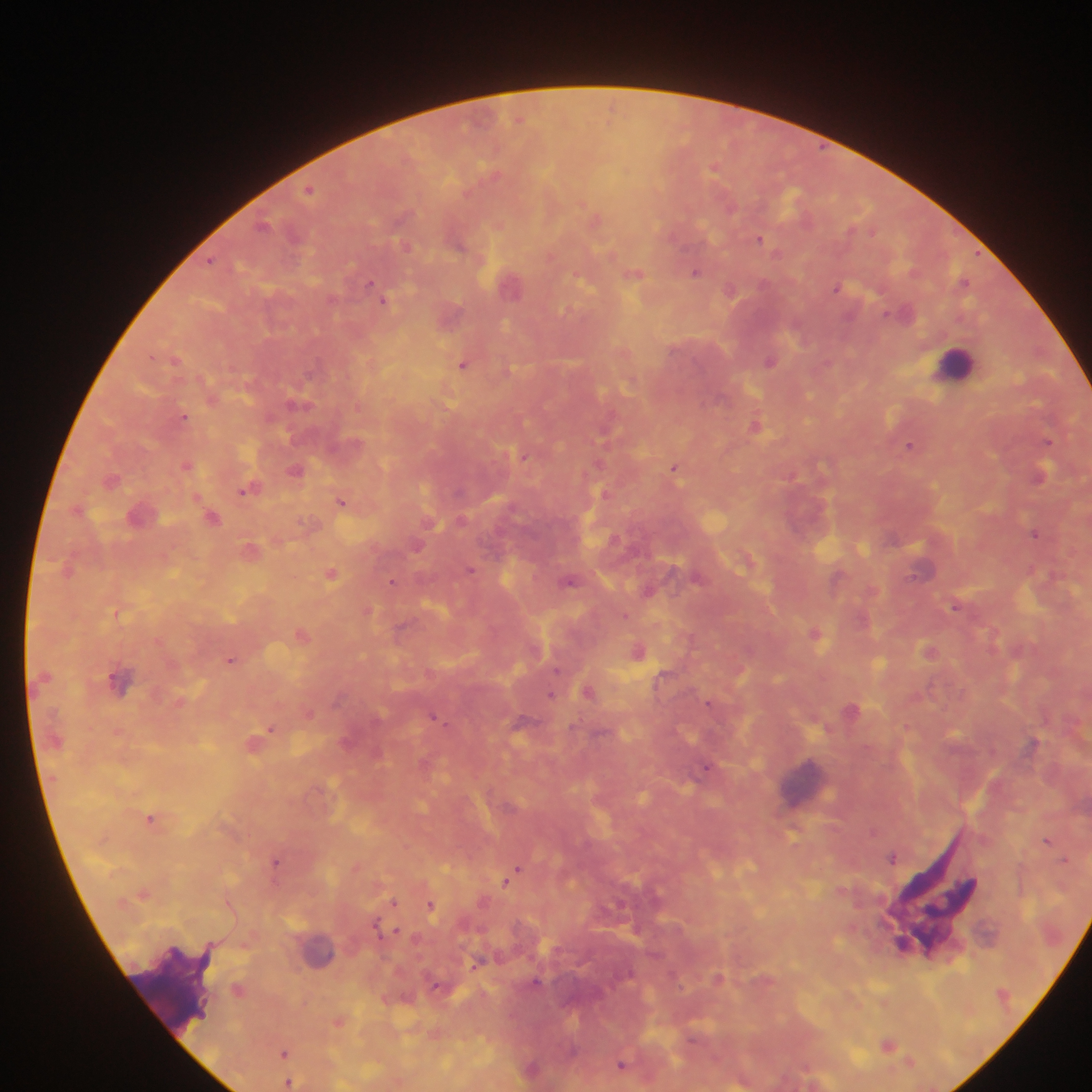

leukocyte locations = approximate centers as [x, y] in pixels: [955, 361], [120, 680], [807, 783], [322, 952], [171, 997]
image size = 1092×1092 pixels
country = Ghana
preparation = thick blood film
Plasmodium parasite locations = approximate centers as [x, y] in pixels: [611, 106], [520, 119], [715, 168], [309, 189], [731, 208], [262, 225], [759, 238], [457, 244], [405, 246], [211, 260], [695, 272], [634, 274], [965, 281], [369, 284], [512, 287], [836, 288], [730, 290], [384, 301], [176, 359], [771, 360], [462, 364], [296, 405], [183, 416], [754, 426], [1047, 441], [909, 446], [524, 456], [187, 465], [674, 467], [295, 470], [1041, 476], [111, 480], [246, 489], [341, 501], [212, 517], [1034, 533], [416, 547], [470, 569], [332, 573], [696, 576], [837, 578], [392, 581], [570, 582], [648, 591], [955, 607], [368, 611], [626, 615], [815, 633], [302, 635], [638, 651], [929, 651], [231, 660], [557, 670], [589, 692], [551, 694], [709, 703], [433, 716], [520, 722], [271, 729], [1033, 743], [706, 767], [149, 818], [873, 831], [1047, 840], [892, 857], [276, 860], [1064, 860], [518, 869], [506, 883], [394, 902], [431, 905], [376, 926], [396, 931], [536, 981], [888, 1044], [284, 1053], [909, 1061], [621, 1065], [288, 1083]
capture = mobile-phone photograph through a microscope
field of view = single